Give the position of every malaria parasite.
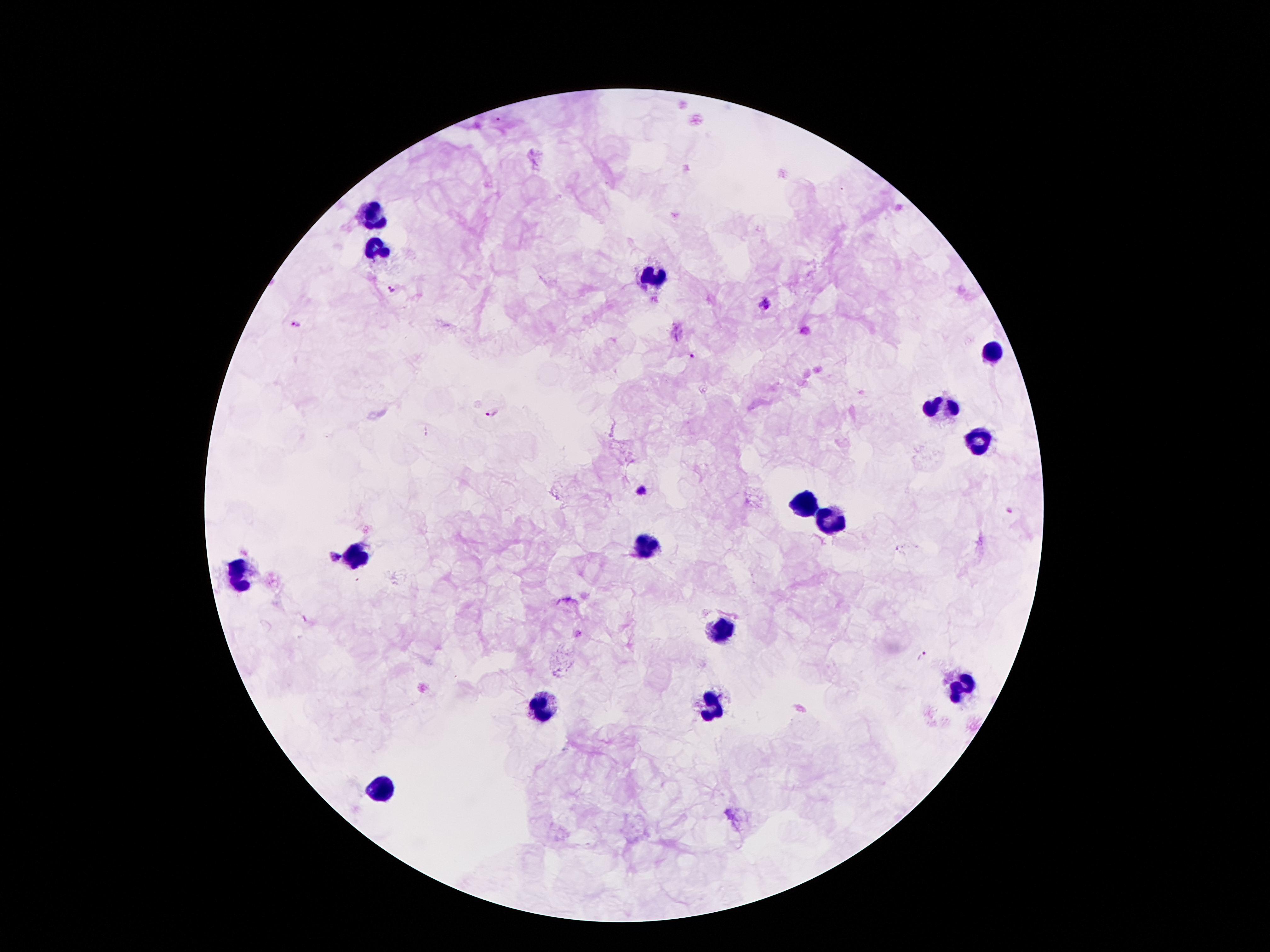
Approximate centers as (x, y) in pixels.
Malaria parasites: (390, 288), (764, 302), (297, 325), (692, 358), (492, 412), (642, 490), (334, 557), (923, 656).

Leukocyte locations: (374, 216), (378, 247), (651, 274), (991, 350), (942, 407), (979, 442), (807, 505), (829, 526), (645, 546), (354, 554), (241, 575), (725, 624), (963, 685), (542, 708), (708, 708), (387, 790). One field from this slide. Thick blood film. 100x magnification. Image is 1270×952 pixels. Patient malaria status: positive for Plasmodium falciparum. Photographed through the microscope eyepiece with a smartphone camera. Giemsa stain.